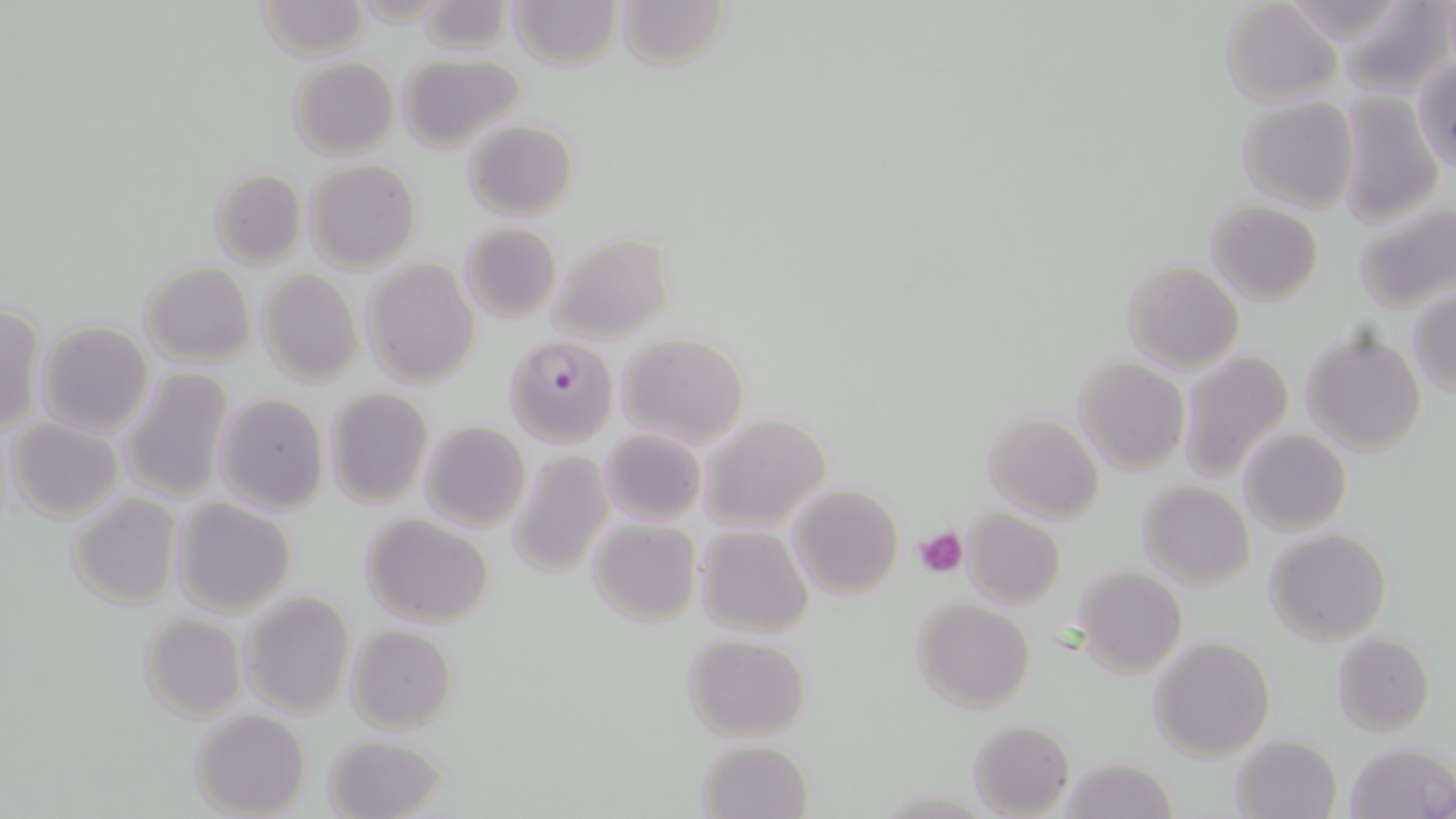
Summary:
  - Coordinate format: approximate bounding boxes as [x1, y1, x2, y2] in pixels
  - Uninfected red blood cell locations: [254, 0, 369, 58], [508, 0, 622, 71], [616, 0, 729, 71], [1277, 0, 1415, 47], [414, 1, 512, 55], [1340, 1, 1455, 97], [1219, 2, 1342, 107], [396, 53, 523, 150], [288, 55, 399, 159], [1412, 56, 1456, 174], [1335, 91, 1443, 226], [1237, 96, 1359, 212], [463, 119, 579, 220], [304, 160, 421, 274], [208, 168, 307, 268], [1353, 199, 1456, 314], [1205, 200, 1325, 306], [459, 222, 561, 323], [547, 232, 673, 344], [361, 258, 481, 390], [1122, 260, 1245, 374], [139, 262, 255, 368], [258, 268, 364, 387], [1409, 288, 1456, 398], [0, 304, 46, 433], [37, 321, 154, 437], [1302, 328, 1427, 457], [614, 332, 750, 449], [1178, 350, 1295, 484], [1073, 354, 1190, 476], [120, 367, 234, 503], [323, 387, 433, 508], [213, 393, 328, 515], [983, 411, 1105, 522], [700, 413, 832, 533], [8, 417, 124, 522], [419, 421, 530, 533], [598, 428, 706, 527], [1238, 428, 1351, 536], [506, 449, 613, 577], [1138, 480, 1254, 589], [788, 483, 904, 599], [67, 493, 181, 608], [173, 498, 297, 615], [961, 507, 1065, 610], [360, 513, 495, 627], [587, 518, 701, 628], [693, 524, 815, 638], [1266, 529, 1391, 645], [1073, 566, 1187, 680], [241, 591, 354, 718], [910, 598, 1035, 713], [138, 612, 247, 722], [345, 624, 457, 734], [1331, 633, 1435, 735], [682, 634, 810, 742], [1148, 635, 1277, 762], [191, 710, 310, 819], [968, 719, 1075, 818], [324, 732, 448, 818], [1231, 735, 1341, 819], [696, 739, 813, 818], [1344, 742, 1455, 819], [1057, 758, 1180, 819]
  - Platelet locations: [916, 526, 968, 578]
  - Plasmodium falciparum-infected red blood cell locations: [504, 336, 618, 448]
  - Slide-level diagnosis: Plasmodium falciparum
  - Modality: optical microscopy
  - Field of view: one of a larger specimen
  - Preparation: thin blood smear
  - Image size: 1456×819 pixels
  - Stain: May-Grünwald-Giemsa
  - Magnification: 1000x